Assess this cell for malaria.
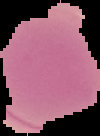

Uninfected.

image type = cell region segmented out of the field of view; surrounding area masked to black
preparation = thin blood smear
image size = 100×136 pixels